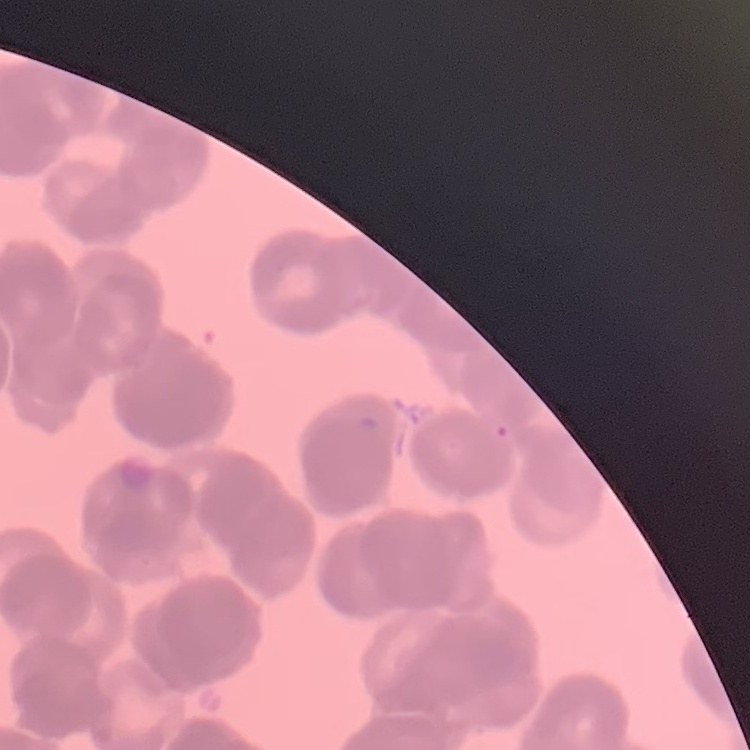

The red blood cells exhibit rouleaux formation. Thin blood smear. One tile cut from a larger photomicrograph. Field's or Giemsa stain.